Describe the morphology of the erythrocytes.
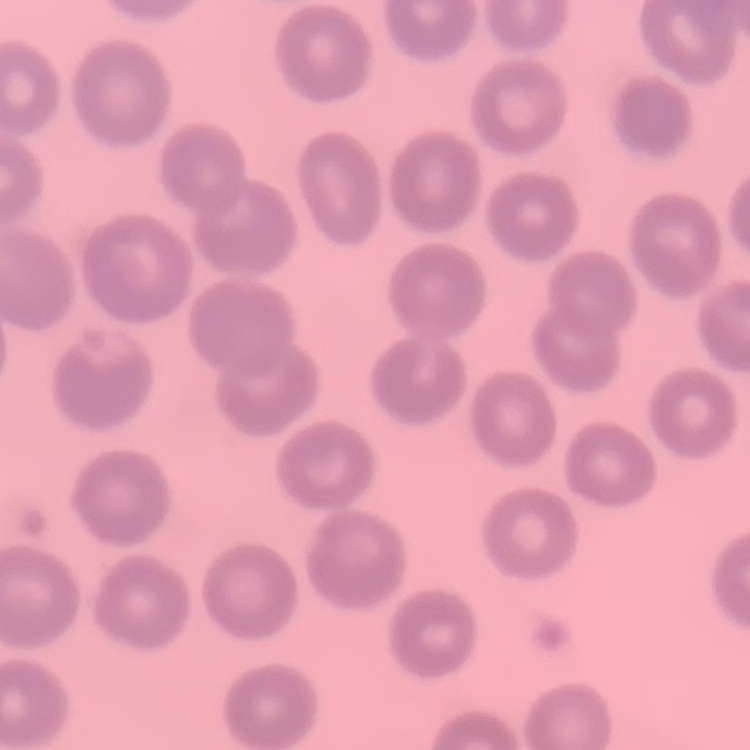

They show no rouleaux formation.

preparation = thin blood smear
stain = Field's or Giemsa
image type = one tile cut from a larger photomicrograph